State which parasite is depicted.
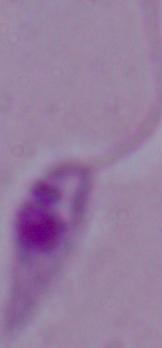
Leishmania.

magnification = 1000x
modality = micrograph